Locate every blood parasite and identify its species.
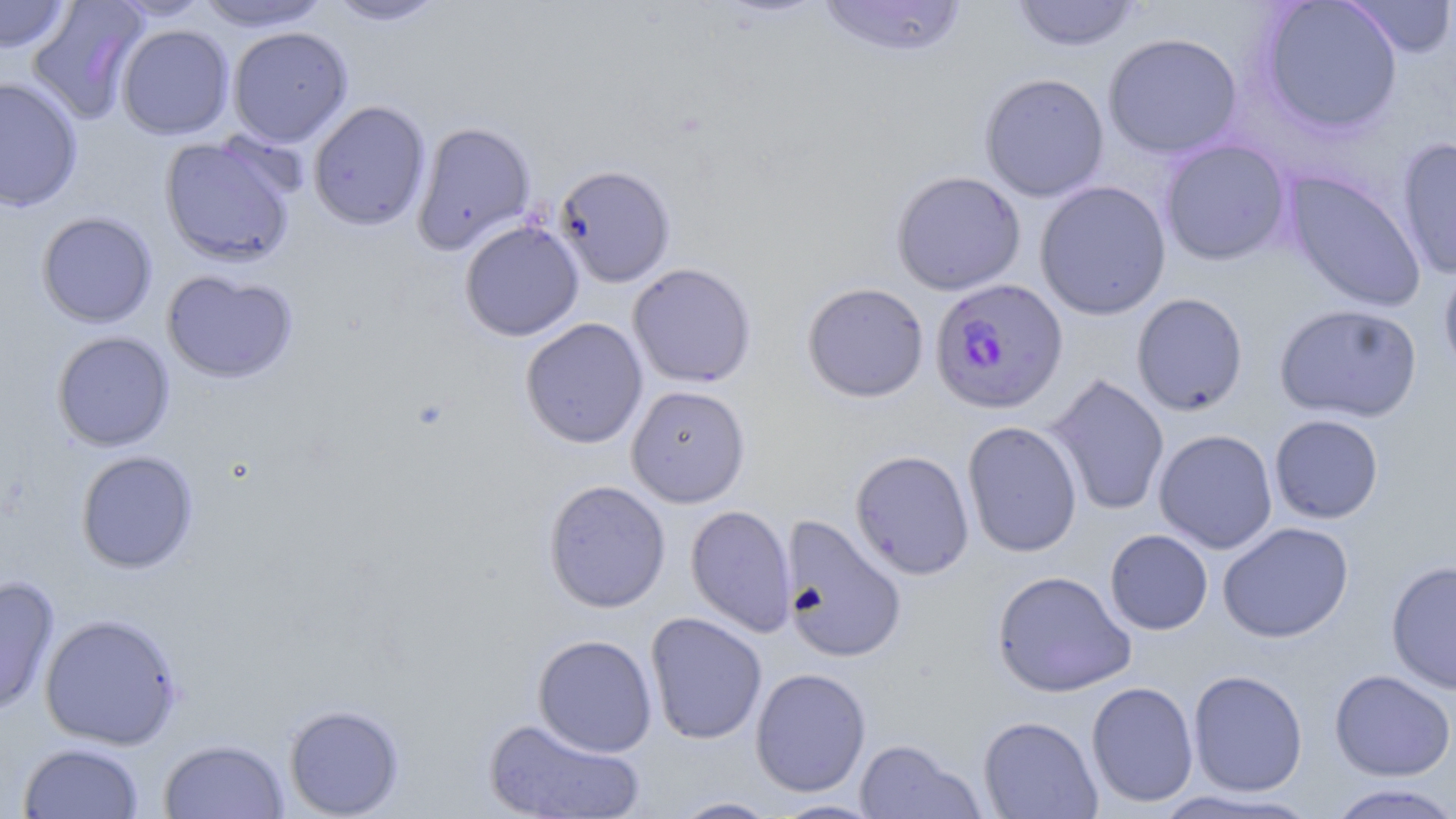

Approximate bounding boxes as (x1, y1, x2, y2) in pixels.
Plasmodium falciparum-infected red blood cells: (929, 277, 1068, 414).
No Plasmodium ovale, Plasmodium malariae, Plasmodium vivax, Babesia divergens, or Trypanosoma brucei observed.

slide-level diagnosis = Plasmodium falciparum
uninfected red blood cell locations = approximate bounding boxes as (x1, y1, x2, y2) in pixels: (107, 0, 213, 21), (193, 0, 332, 32), (325, 0, 447, 26), (815, 0, 968, 58), (1009, 0, 1143, 52), (0, 1, 73, 53), (26, 1, 149, 124), (1258, 1, 1403, 135), (1341, 1, 1456, 57), (116, 24, 235, 140), (227, 26, 353, 147), (1102, 32, 1243, 159), (979, 72, 1109, 202), (0, 77, 83, 211), (308, 100, 431, 231), (412, 121, 536, 255), (159, 134, 300, 268), (1396, 137, 1456, 280), (1159, 139, 1292, 266), (553, 164, 676, 288), (891, 170, 1026, 295), (1283, 171, 1427, 312), (1035, 180, 1172, 320), (36, 211, 158, 328), (459, 219, 584, 342), (1438, 260, 1456, 384), (627, 263, 757, 388), (162, 270, 298, 384), (802, 281, 929, 403), (1131, 293, 1249, 416), (1274, 303, 1423, 423), (520, 317, 648, 449), (51, 331, 175, 452), (1047, 374, 1170, 516), (626, 385, 751, 508), (1269, 414, 1384, 524), (962, 420, 1083, 558), (1154, 429, 1278, 553), (850, 449, 975, 579), (76, 450, 199, 574), (543, 479, 671, 613), (685, 504, 797, 637), (779, 515, 907, 663), (1216, 522, 1354, 643), (1105, 529, 1213, 635), (1386, 559, 1456, 696), (991, 570, 1135, 697), (0, 575, 60, 716), (645, 612, 767, 745), (39, 613, 183, 749), (533, 633, 657, 757), (750, 667, 871, 797), (1187, 669, 1308, 797), (1329, 669, 1456, 781), (1086, 681, 1198, 808), (283, 703, 404, 817), (978, 715, 1102, 818), (483, 717, 646, 818), (158, 738, 289, 819), (854, 739, 983, 819), (18, 742, 144, 818), (1324, 783, 1456, 819), (1152, 790, 1319, 818), (669, 797, 781, 818), (768, 799, 884, 818)
field of view = single
modality = light microscopy
preparation = thin blood smear
stain = May-Grünwald-Giemsa
magnification = 1000x
image size = 1456×819 pixels